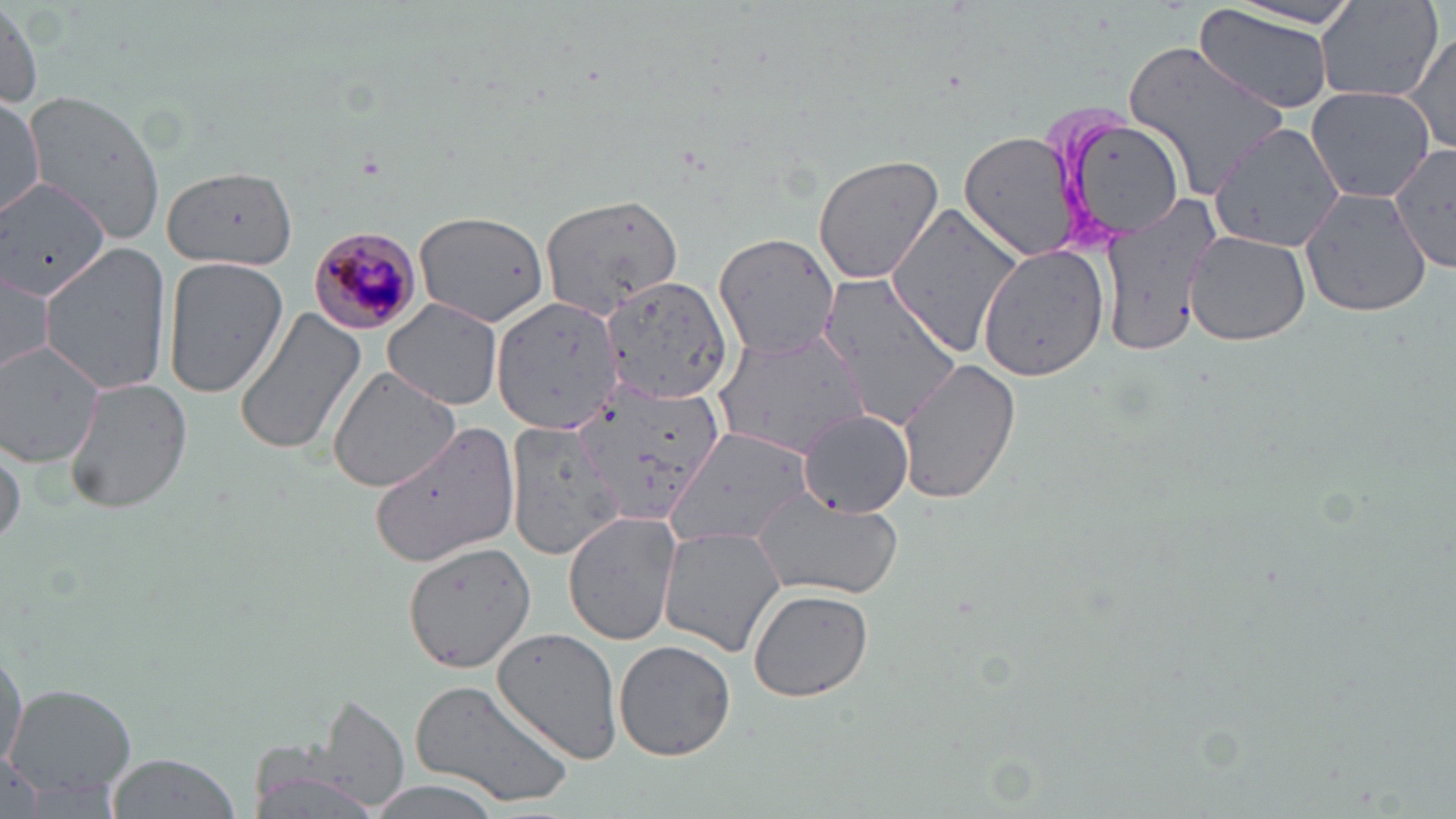 Approximate bounding boxes as (x1,y1)-(x2,y2) corner pairs in pixels. Plasmodium malariae-infected red blood cell locations: (309,225)-(424,336). Uninfected red blood cell locations: (1314,1)-(1444,102), (1227,2)-(1364,30), (2,4)-(41,111), (1195,5)-(1338,114), (1403,31)-(1455,156), (1123,38)-(1289,197), (0,83)-(105,227), (1306,86)-(1434,203), (25,91)-(166,243), (0,92)-(45,219), (1051,110)-(1191,248), (1206,116)-(1345,265), (959,129)-(1080,262), (1386,138)-(1453,280), (811,154)-(946,285), (161,165)-(298,271), (0,182)-(109,301), (1300,186)-(1435,318), (540,194)-(683,320), (1095,196)-(1222,360), (883,205)-(1025,362), (415,211)-(552,328), (1185,230)-(1311,348), (713,232)-(841,358), (40,241)-(172,397), (978,245)-(1110,380), (161,257)-(290,399), (0,264)-(55,375), (819,271)-(964,427), (598,277)-(738,403), (491,294)-(625,433), (383,298)-(504,410), (232,307)-(368,459), (711,326)-(872,460), (1,338)-(106,466), (897,356)-(1022,506), (327,367)-(460,495), (66,377)-(191,514), (568,382)-(725,527), (802,410)-(912,517), (505,416)-(625,561), (370,420)-(520,566), (667,426)-(811,548), (1,436)-(25,552), (749,493)-(900,599), (564,510)-(683,647), (658,526)-(785,656), (401,539)-(539,672), (747,587)-(874,702), (492,625)-(627,765), (614,639)-(736,761), (0,642)-(27,773), (408,677)-(576,808), (5,684)-(136,807), (303,693)-(413,815), (246,725)-(395,819), (106,752)-(241,819), (358,778)-(506,818). Slide-level diagnosis: Plasmodium malariae. Single field of view. 1000x magnification. May-Grünwald-Giemsa stain. Image is 1456×819 pixels. Thin blood smear. Optical microscopy.